Locate every Plasmodium parasite.
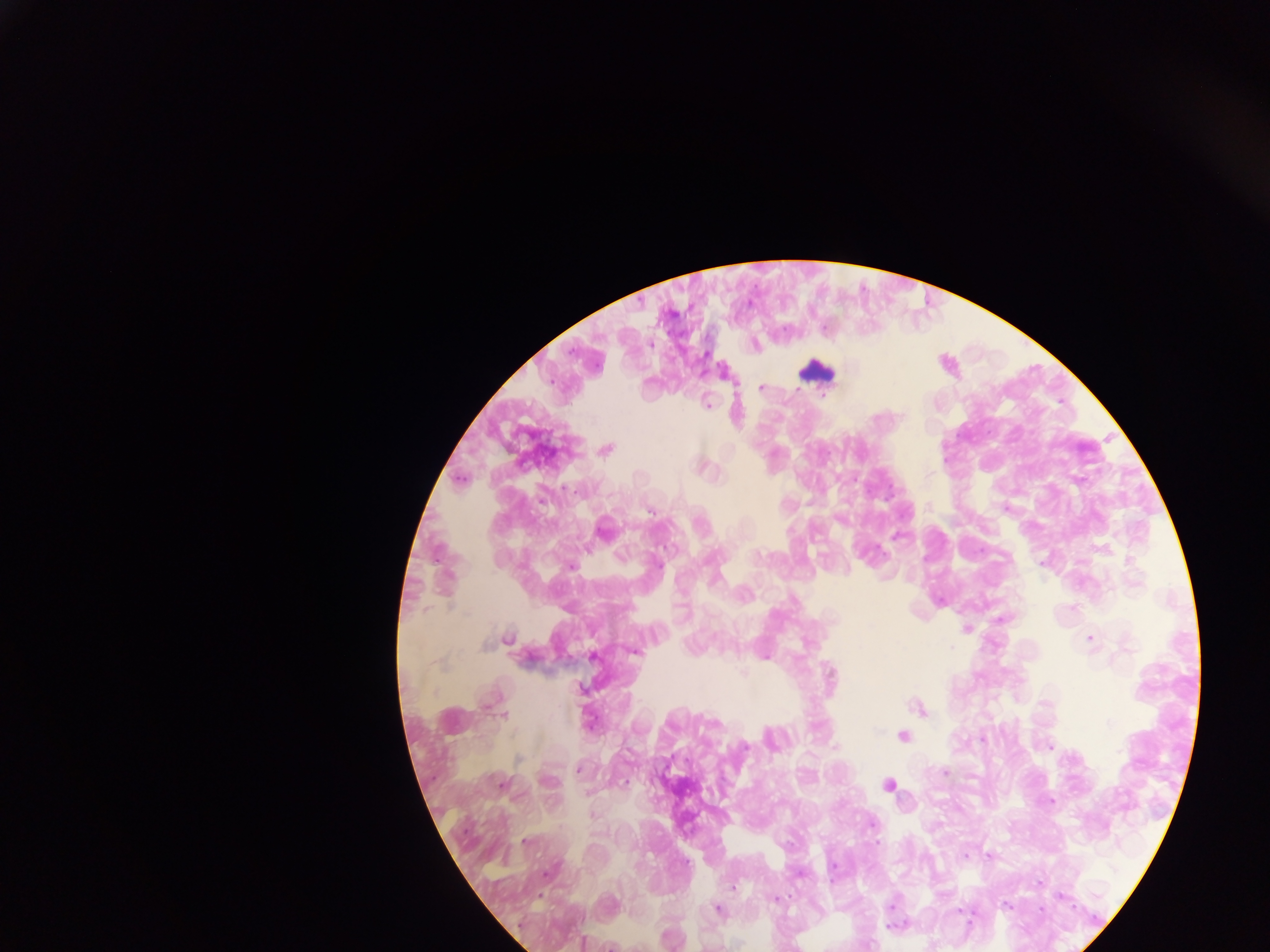
Approximate centers as {x, y} in pixels.
Plasmodium parasites: {756, 344}, {764, 385}, {708, 402}, {738, 412}, {607, 447}, {705, 463}, {462, 478}, {899, 534}, {941, 599}, {968, 628}, {1092, 638}, {637, 651}, {766, 653}, {922, 707}, {505, 713}, {984, 738}, {1051, 746}, {519, 757}, {579, 768}, {505, 783}, {589, 792}, {1051, 799}, {594, 813}, {548, 873}, {541, 895}, {777, 897}, {894, 905}, {720, 908}, {584, 940}, {932, 944}.

country = Ghana
image size = 1270×952 pixels
capture = mobile-phone photograph through a microscope
field of view = single
leukocyte locations = approximate centers as {x, y} in pixels: {950, 362}, {728, 369}, {817, 369}, {606, 527}, {903, 734}, {890, 783}
preparation = thick blood film